Report the malaria status of this cell.
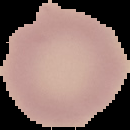

It is uninfected.

Image is 130×130 pixels. From a thin blood film. Segmented cell region on a black background.